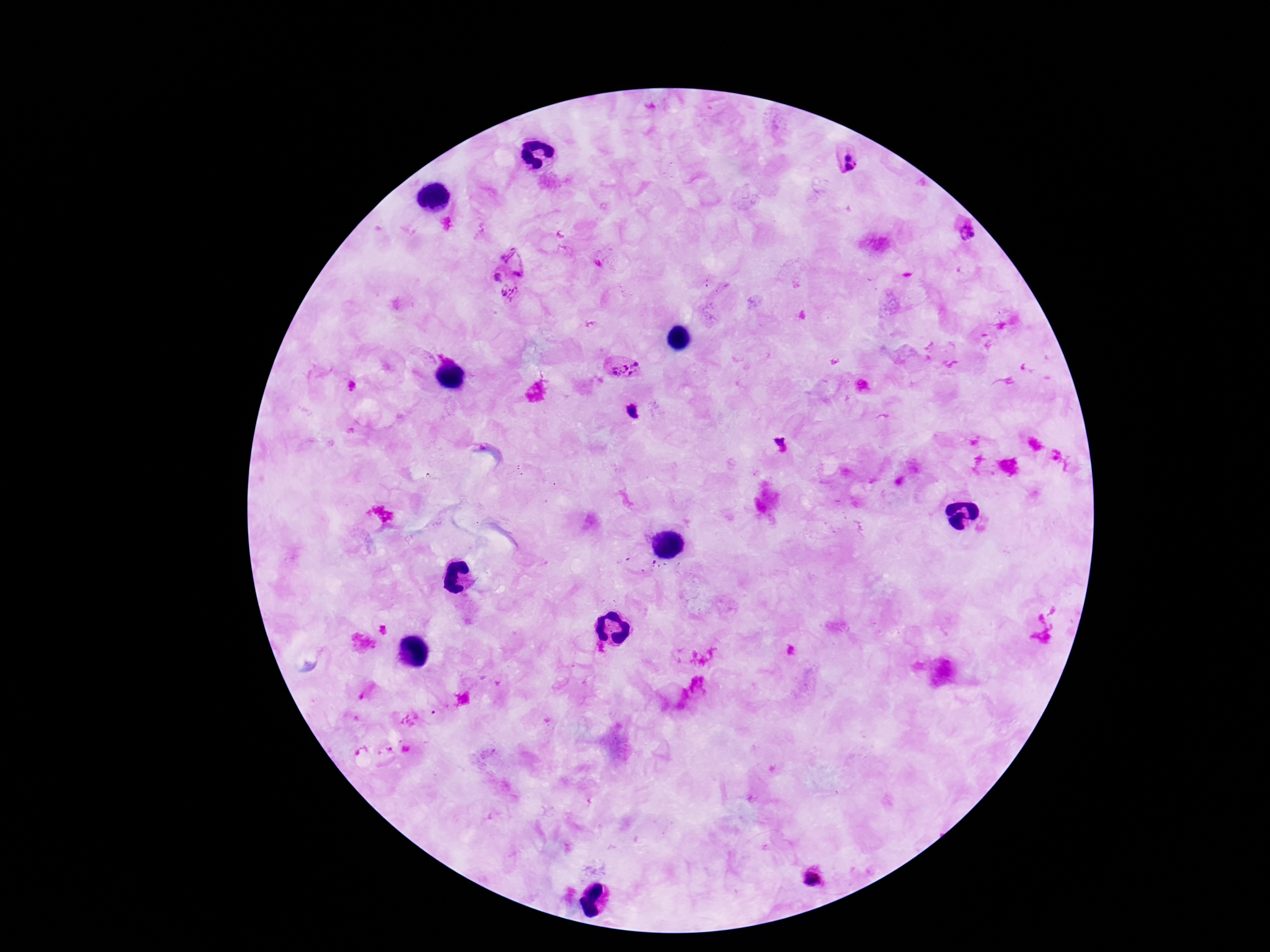
capture = smartphone camera through the microscope eyepiece
stain = Giemsa
Plasmodium parasite locations = approximate centers as [x, y] in pixels: [848, 156], [856, 162], [848, 168], [962, 231], [516, 259], [496, 278], [510, 292], [624, 367], [632, 410], [781, 445], [813, 877]
patient malaria status = infected
magnification = 100x
preparation = thick blood film
field of view = single
image size = 1270×952 pixels